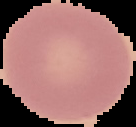
image size = 136×127 pixels
preparation = thin blood film
image type = segmented cell region with the area outside set to black
result = no Plasmodium parasites detected